Locate every blood parasite and identify its species.
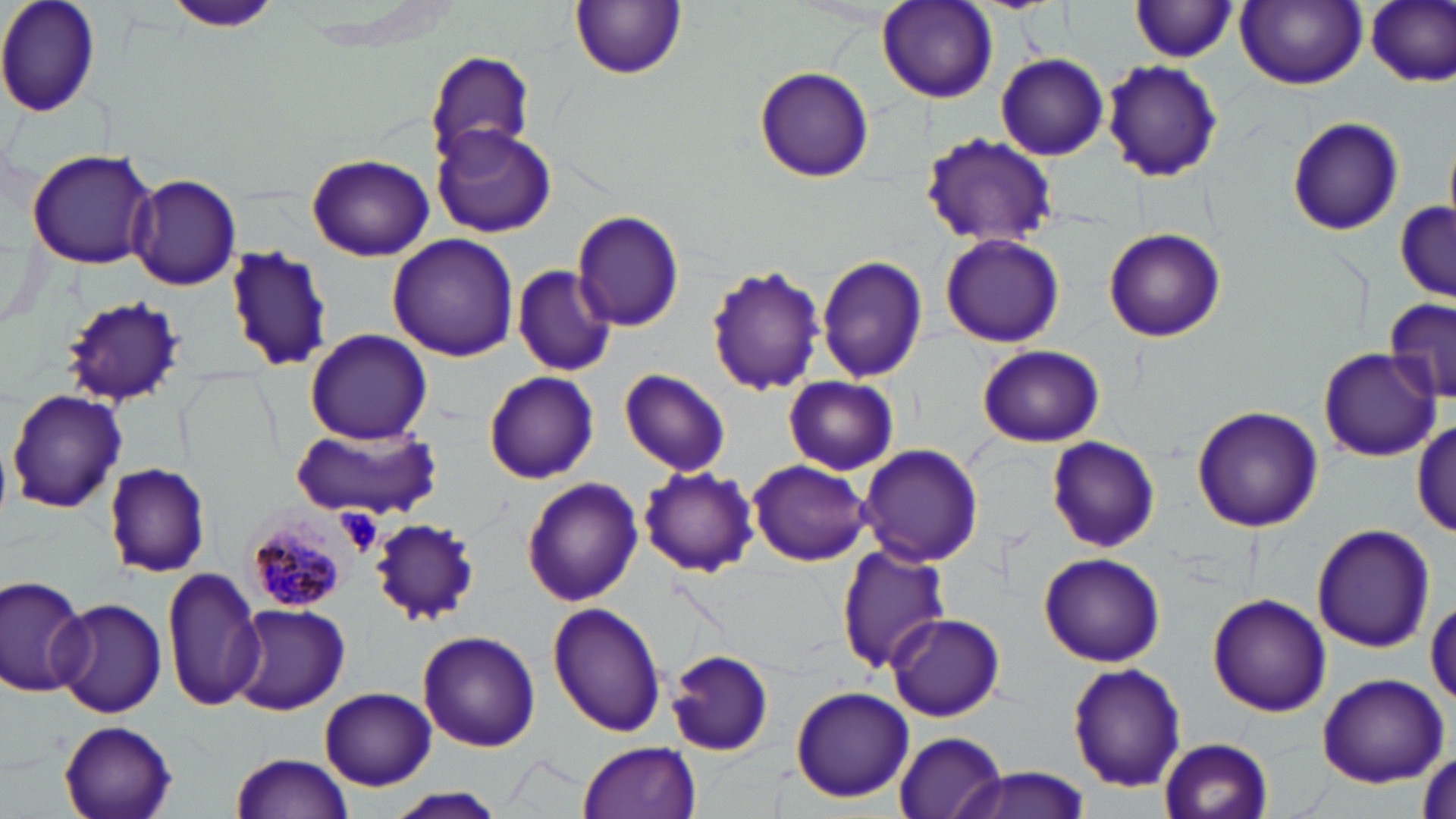
Approximate bounding boxes as [x1, y1, x2, y2] in pixels.
Plasmodium malariae-infected red blood cells: [237, 503, 360, 613].
No Plasmodium falciparum, Plasmodium ovale, Plasmodium vivax, Babesia divergens, or Trypanosoma brucei observed.

Platelet locations: [335, 507, 383, 557]. Uninfected red blood cell locations: [0, 0, 102, 119], [570, 0, 687, 80], [1235, 0, 1367, 89], [1365, 0, 1455, 87], [166, 1, 287, 34], [877, 1, 998, 104], [1130, 1, 1238, 63], [423, 48, 534, 169], [997, 54, 1108, 160], [1101, 57, 1223, 183], [752, 65, 876, 184], [1287, 116, 1405, 236], [431, 123, 558, 238], [918, 131, 1061, 250], [26, 147, 156, 270], [307, 152, 436, 259], [127, 174, 242, 290], [1393, 201, 1454, 302], [574, 210, 686, 331], [1103, 227, 1226, 344], [940, 233, 1065, 348], [387, 234, 518, 361], [224, 246, 330, 371], [816, 254, 929, 384], [705, 264, 827, 398], [512, 266, 616, 377], [57, 294, 183, 406], [1383, 297, 1453, 407], [305, 328, 434, 443], [978, 344, 1105, 448], [1319, 348, 1438, 461], [619, 369, 730, 477], [485, 372, 599, 483], [783, 376, 899, 475], [8, 389, 127, 513], [1191, 405, 1323, 534], [1413, 417, 1455, 540], [291, 426, 441, 519], [1044, 437, 1159, 550], [857, 444, 984, 567], [747, 459, 871, 566], [103, 462, 211, 577], [638, 464, 759, 576], [522, 478, 643, 607], [370, 516, 479, 625], [1311, 523, 1435, 653], [837, 544, 951, 673], [1038, 551, 1166, 666], [162, 569, 261, 709], [0, 573, 93, 696], [1208, 594, 1330, 716], [51, 597, 168, 719], [549, 603, 666, 738], [229, 605, 349, 714], [885, 612, 1009, 722], [407, 623, 660, 744], [416, 630, 541, 753], [665, 649, 772, 756], [1067, 662, 1186, 792], [1315, 673, 1449, 787], [789, 685, 915, 803], [319, 687, 437, 790], [57, 718, 179, 819], [891, 731, 1006, 819], [1158, 737, 1274, 819], [578, 741, 701, 819], [230, 754, 354, 819], [949, 767, 1094, 819], [383, 787, 511, 819]. Slide-level diagnosis: Plasmodium malariae. May-Grünwald-Giemsa-stained preparation. Image is 1456×819 pixels. Light microscopy. Captured at 1000x magnification. One field of a larger specimen. Thin blood smear.